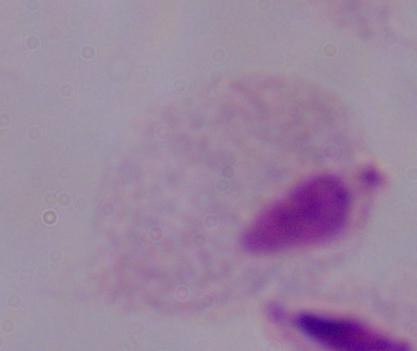
Summary:
  - Magnification: 1000x
  - Modality: photomicrograph
  - Identification: trichomonad